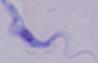

identification = trypanosome
magnification = 1000x
modality = photomicrograph